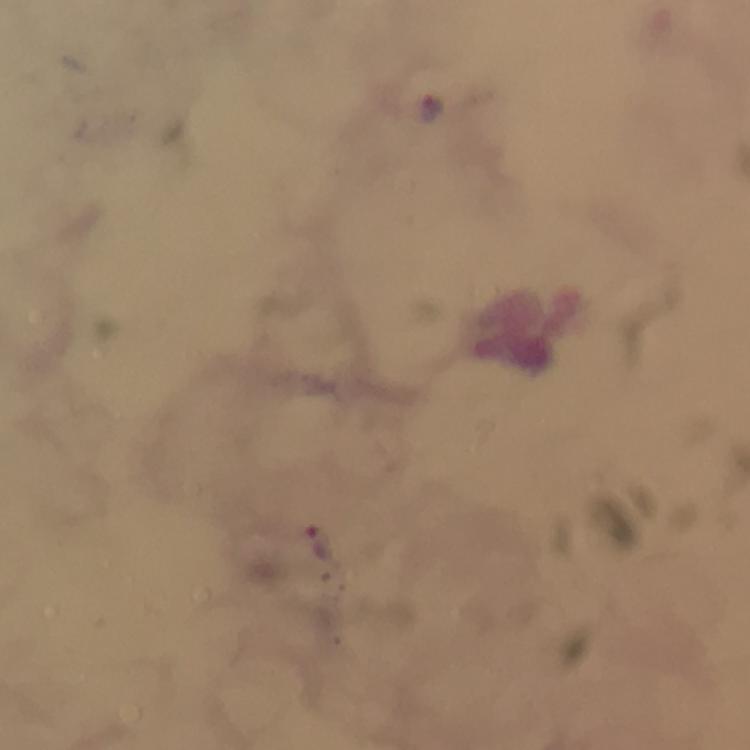
image size = 750×750 pixels
context = from a malaria diagnostic workup
malaria parasite locations = approximate centers as {x, y} in pixels: {431, 106}, {319, 542}
stain = Giemsa
immersion oil = applied
preparation = thick blood film
capture = smartphone camera through the microscope
cropped from = a single field of view
magnification = 100x